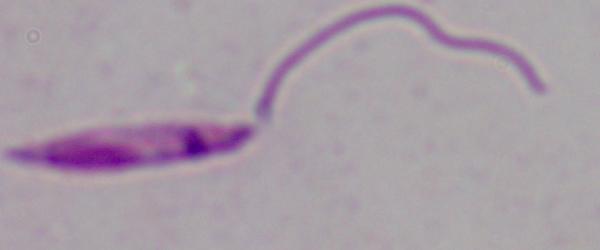

Summary:
  - Modality: photomicrograph
  - Magnification: 1000x
  - Identification: Leishmania